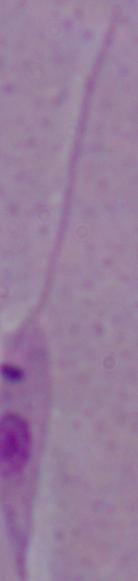

A Leishmania parasite is shown. Micrograph. 1000x magnification.